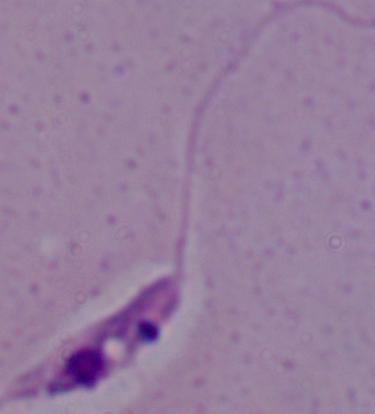

magnification = 1000x
identification = Leishmania
modality = micrograph